Assess the morphology of the red blood cells.
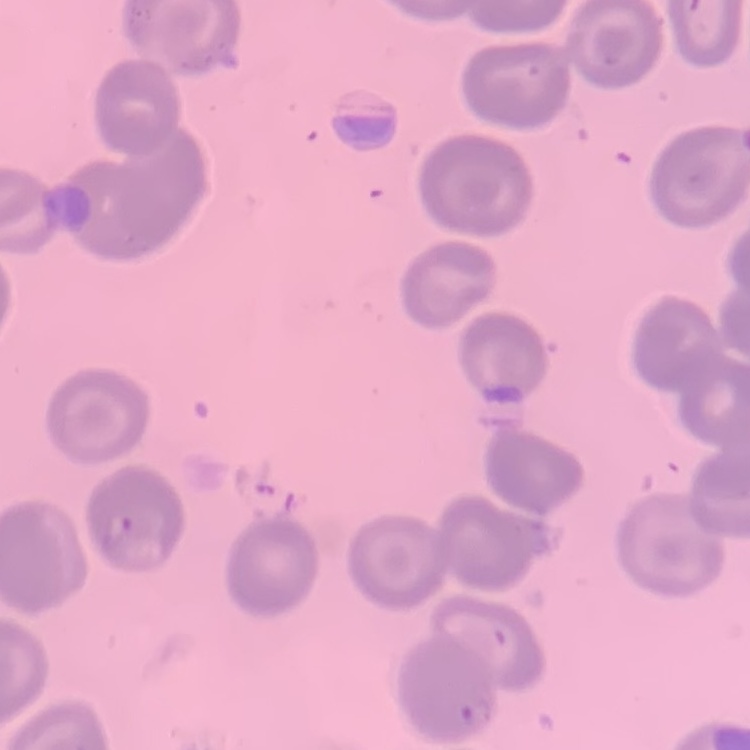
They show no rouleaux formation.

preparation: thin blood film
image_type: one tile cut from a larger photomicrograph
stain: Field's or Giemsa